Locate every blood parasite and identify its species.
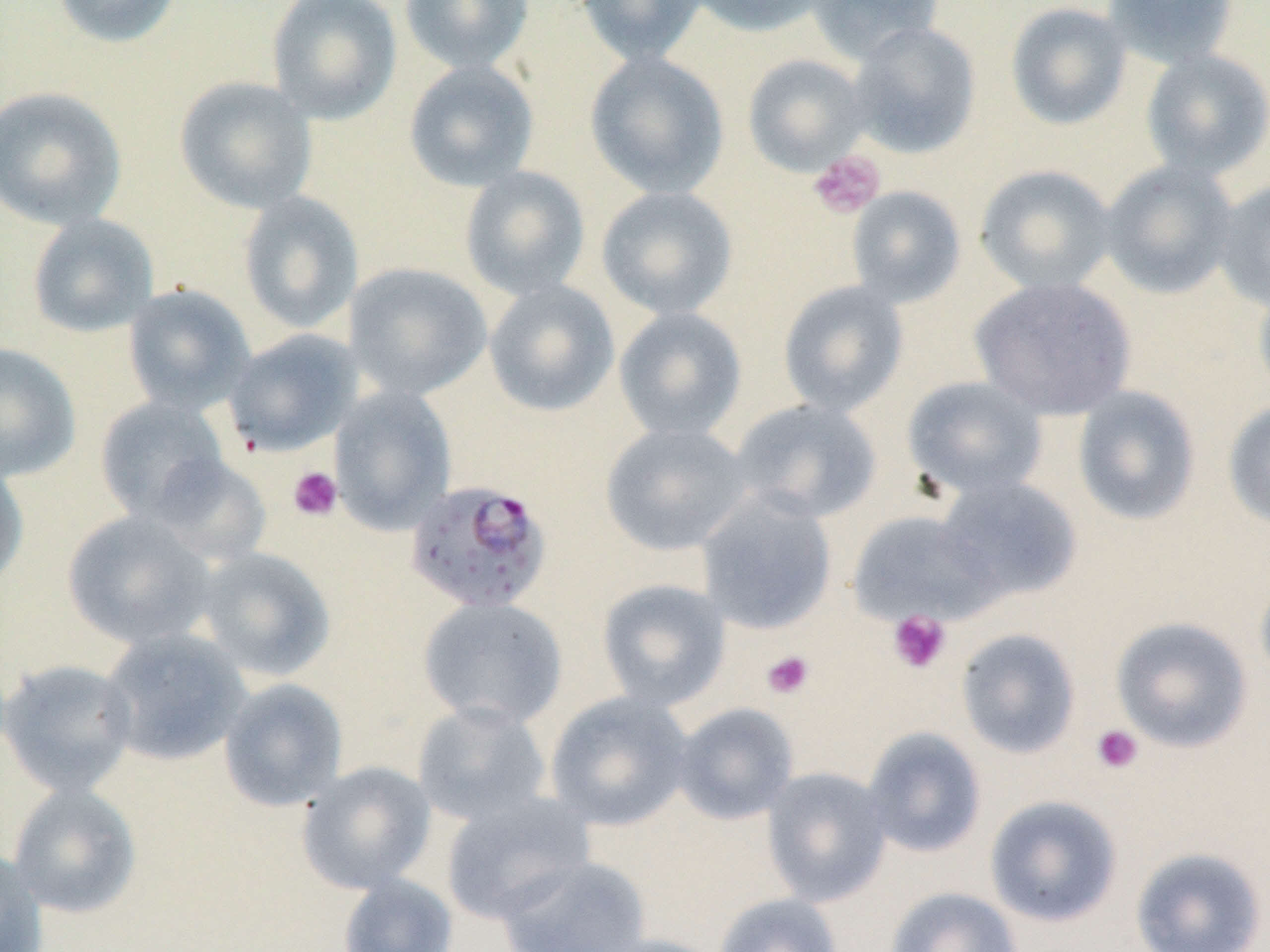

Approximate bounding boxes as named x1/y1/x2/y2 corners in pixels.
Plasmodium falciparum-infected red blood cells: (x1=405, y1=480, x2=553, y2=616).
No Plasmodium ovale, Plasmodium malariae, Plasmodium vivax, Babesia divergens, or Trypanosoma brucei observed.

Uninfected red blood cell locations: (x1=52, y1=0, x2=183, y2=49), (x1=266, y1=0, x2=402, y2=125), (x1=399, y1=0, x2=534, y2=74), (x1=574, y1=0, x2=707, y2=66), (x1=684, y1=0, x2=834, y2=37), (x1=804, y1=0, x2=943, y2=64), (x1=1101, y1=0, x2=1239, y2=70), (x1=1005, y1=2, x2=1133, y2=130), (x1=846, y1=21, x2=982, y2=159), (x1=1139, y1=49, x2=1270, y2=180), (x1=585, y1=51, x2=730, y2=199), (x1=741, y1=53, x2=871, y2=176), (x1=403, y1=60, x2=540, y2=192), (x1=174, y1=76, x2=317, y2=214), (x1=0, y1=86, x2=127, y2=230), (x1=1099, y1=160, x2=1239, y2=299), (x1=975, y1=164, x2=1117, y2=294), (x1=459, y1=166, x2=591, y2=300), (x1=1213, y1=177, x2=1270, y2=313), (x1=596, y1=186, x2=738, y2=319), (x1=845, y1=186, x2=967, y2=308), (x1=238, y1=191, x2=363, y2=335), (x1=26, y1=213, x2=159, y2=338), (x1=344, y1=262, x2=492, y2=401), (x1=969, y1=276, x2=1136, y2=420), (x1=1253, y1=278, x2=1270, y2=406), (x1=483, y1=279, x2=620, y2=417), (x1=777, y1=280, x2=910, y2=417), (x1=122, y1=283, x2=255, y2=415), (x1=613, y1=306, x2=748, y2=442), (x1=225, y1=328, x2=362, y2=457), (x1=0, y1=343, x2=81, y2=482), (x1=901, y1=375, x2=1049, y2=501), (x1=1071, y1=386, x2=1201, y2=526), (x1=329, y1=387, x2=457, y2=533), (x1=95, y1=396, x2=230, y2=523), (x1=1222, y1=398, x2=1270, y2=532), (x1=729, y1=399, x2=883, y2=524), (x1=600, y1=422, x2=753, y2=556), (x1=150, y1=455, x2=273, y2=566), (x1=0, y1=458, x2=30, y2=591), (x1=933, y1=476, x2=1083, y2=605), (x1=696, y1=490, x2=838, y2=635), (x1=847, y1=509, x2=1000, y2=625), (x1=62, y1=510, x2=216, y2=649), (x1=194, y1=546, x2=336, y2=682), (x1=1255, y1=569, x2=1270, y2=692), (x1=596, y1=578, x2=731, y2=711), (x1=417, y1=596, x2=568, y2=730), (x1=1110, y1=616, x2=1254, y2=754), (x1=99, y1=626, x2=251, y2=767), (x1=955, y1=628, x2=1081, y2=759), (x1=1, y1=659, x2=139, y2=797), (x1=218, y1=678, x2=348, y2=812), (x1=544, y1=691, x2=695, y2=832), (x1=411, y1=700, x2=552, y2=827), (x1=671, y1=702, x2=799, y2=825), (x1=861, y1=727, x2=987, y2=858), (x1=296, y1=760, x2=437, y2=894), (x1=761, y1=766, x2=893, y2=907), (x1=7, y1=783, x2=142, y2=918), (x1=439, y1=791, x2=595, y2=924), (x1=984, y1=794, x2=1122, y2=927), (x1=0, y1=845, x2=48, y2=952), (x1=1129, y1=846, x2=1267, y2=951), (x1=495, y1=855, x2=651, y2=951), (x1=337, y1=873, x2=458, y2=952), (x1=885, y1=886, x2=1022, y2=952), (x1=713, y1=893, x2=843, y2=952), (x1=588, y1=934, x2=728, y2=952). Platelet locations: (x1=808, y1=150, x2=886, y2=219), (x1=287, y1=466, x2=343, y2=521), (x1=887, y1=610, x2=951, y2=674), (x1=761, y1=650, x2=815, y2=699), (x1=1091, y1=724, x2=1144, y2=774). Slide-level diagnosis: Plasmodium falciparum. May-Grünwald-Giemsa stain. Thin blood smear. Captured at 1000x magnification. Light microscopy. Image is 1270×952 pixels. Single field of view.